Comment on the morphology of the red blood cells.
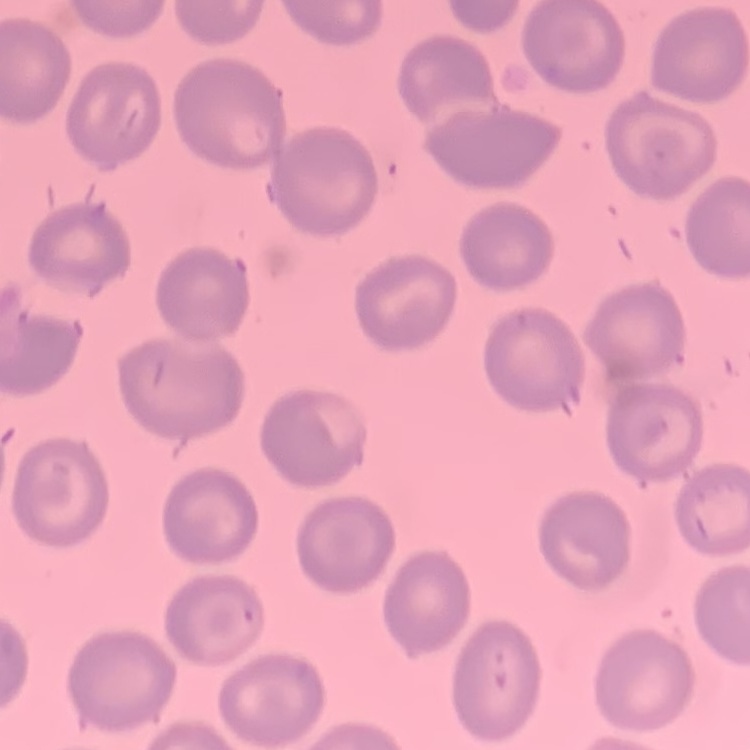
They show no rouleaux formation.

Summary:
  - Preparation: thin blood smear
  - Image type: square crop of a larger photomicrograph
  - Stain: Field's or Giemsa